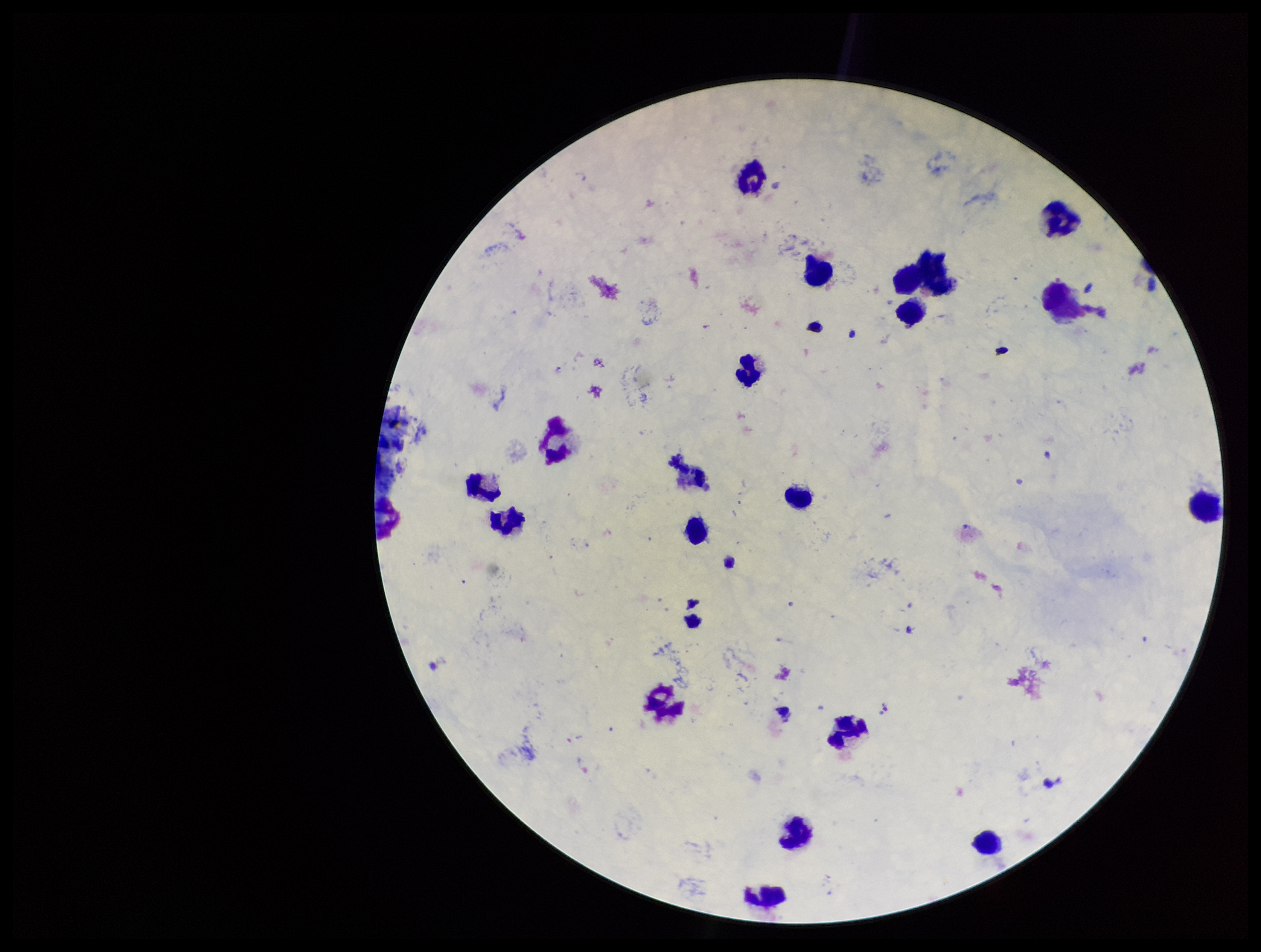
Stained with Giemsa. Plasmodium parasites: seen. One field from this slide. Species reported for this patient: Plasmodium vivax. Image is 1261×952 pixels. Patient malaria status: infected. Parasite count: 1. Leukocyte count: 18. Preparation: thick. Photographed through the microscope eyepiece with a smartphone camera.